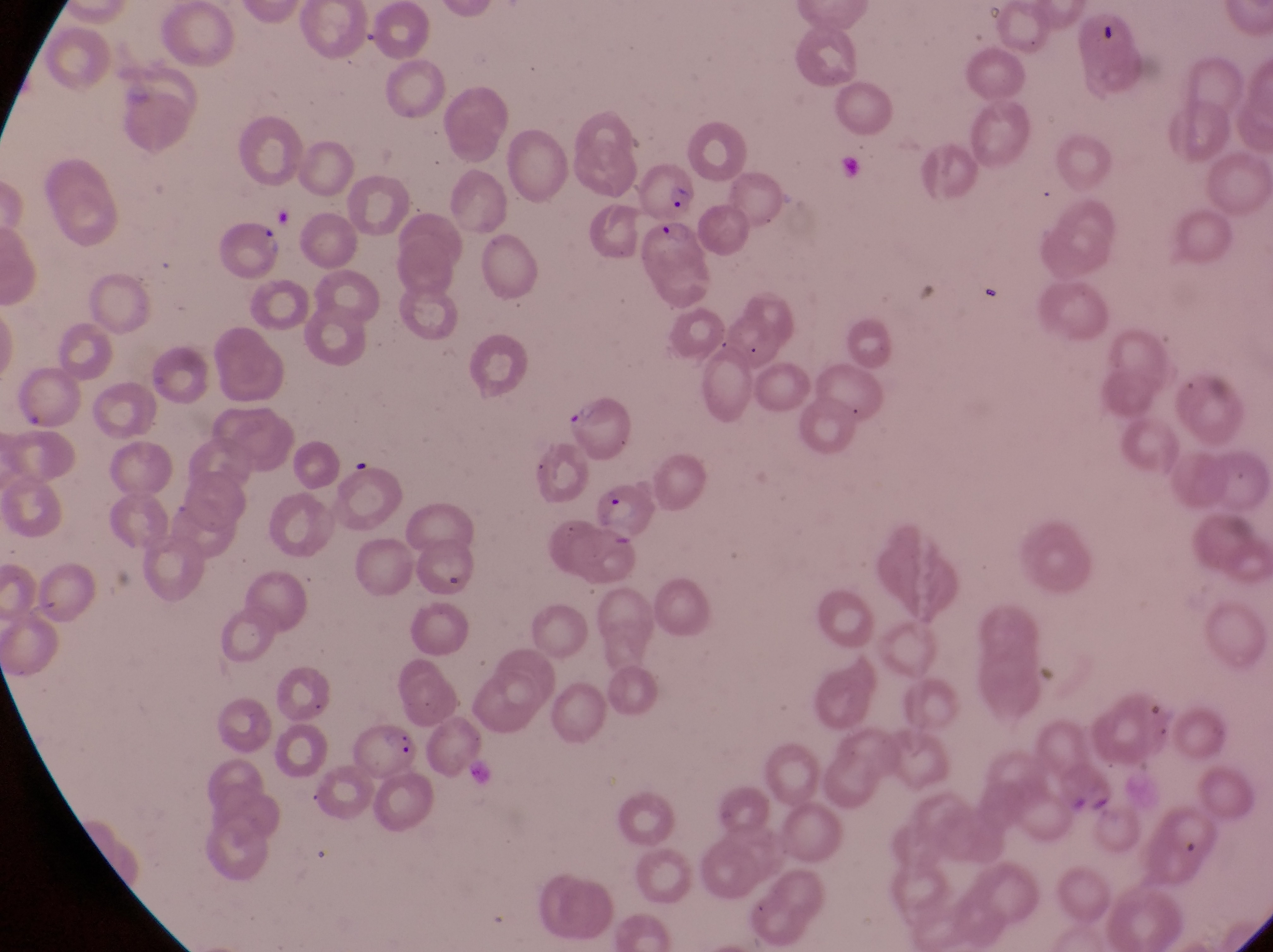
country = Uganda
magnification = 1000x
parasitised red blood cell locations = approximate bounding boxes as [left, top, right, bottom] in pixels: [642, 152, 695, 222], [641, 215, 715, 300], [217, 218, 284, 280], [559, 398, 633, 458], [594, 472, 656, 537], [347, 721, 425, 783]
image size = 1273×952 pixels
preparation = thin blood film
capture = smartphone photograph through the eyepiece of an Olympus CX-23 microscope
field of view = single